State which parasite is depicted.
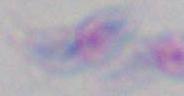

This is Toxoplasma gondii.

1000x magnification. Micrograph.